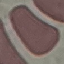

Result: no malaria parasites seen. Acquired by smartphone through the microscope eyepiece. Automatically extracted cell patch, resized to 64 × 64 pixels. Giemsa-stained preparation. Thin smear of blood.